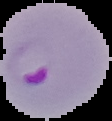

Summary:
  - Preparation: thin blood film
  - Image size: 112×121 pixels
  - Malaria status: parasitized
  - Image type: cell region segmented out of the field of view; surrounding area masked to black